Classify this cell by malaria status.
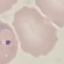
It is parasitized.

Summary:
  - Capture: smartphone camera at the microscope eyepiece
  - Stain: Giemsa
  - Image type: automatically extracted cell patch, resized to 64 × 64 pixels
  - Preparation: thin blood smear